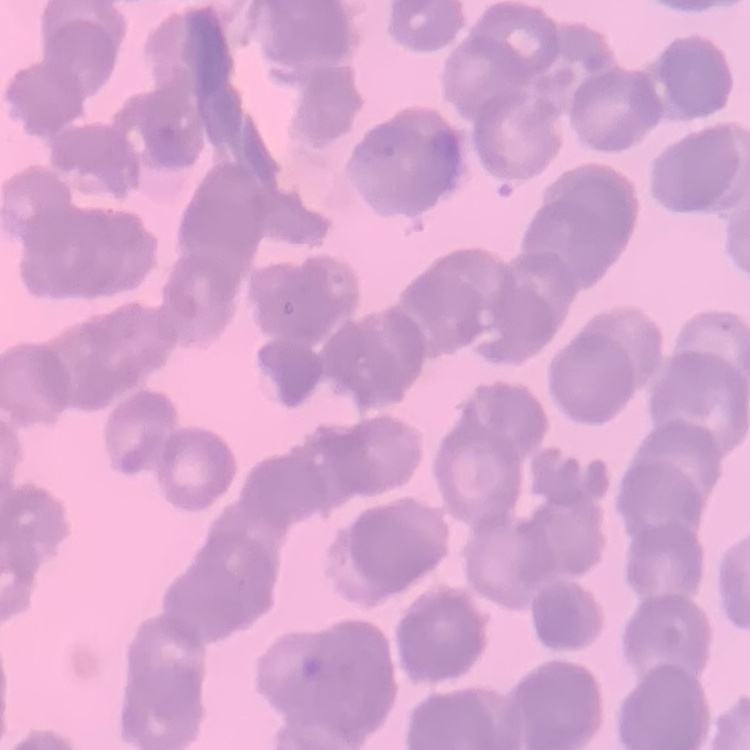
erythrocyte morphology = rouleaux formation
preparation = thin blood film
image type = square crop of a larger photomicrograph
stain = Field's or Giemsa